State which parasite is depicted.
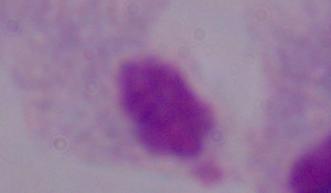
This is a trichomonad.

Summary:
  - Magnification: 1000x
  - Modality: photomicrograph